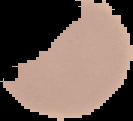

Summary:
  - Image type: segmented cell region on a black background
  - Preparation: thin blood smear
  - Malaria status: uninfected
  - Image size: 133×121 pixels